Point out every malaria parasite.
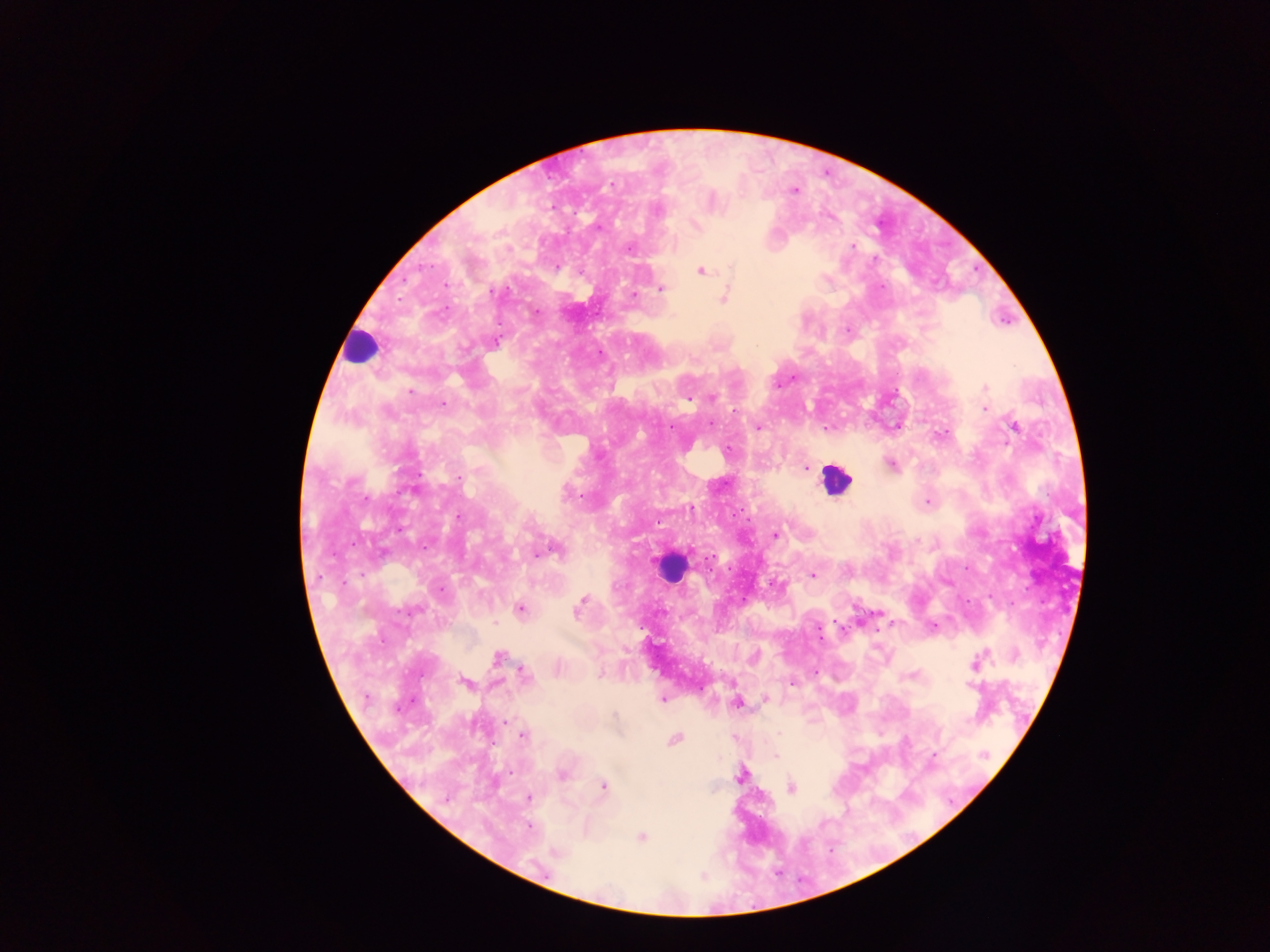
Approximate centers as {x, y} in pixels.
Malaria parasites: {795, 191}, {658, 211}, {695, 225}, {853, 246}, {628, 248}, {557, 267}, {700, 271}, {661, 289}, {633, 295}, {724, 298}, {537, 311}, {846, 330}, {496, 342}, {985, 388}, {410, 390}, {713, 398}, {687, 399}, {443, 404}, {985, 408}, {1014, 426}, {758, 428}, {728, 450}, {891, 464}, {805, 467}, {459, 478}, {413, 489}, {566, 494}, {927, 502}, {459, 517}, {776, 534}, {556, 551}, {537, 555}, {712, 558}, {812, 574}, {441, 589}, {583, 599}, {520, 609}, {412, 610}, {577, 612}, {933, 627}, {497, 658}, {974, 663}, {524, 672}, {815, 672}, {601, 673}, {465, 682}, {792, 683}, {971, 684}, {663, 699}, {765, 699}, {737, 703}, {615, 715}, {506, 722}, {779, 733}, {522, 736}, {674, 739}, {934, 754}, {775, 755}, {985, 755}, {561, 774}, {739, 776}, {604, 785}, {791, 788}, {528, 798}, {530, 827}, {641, 837}, {557, 852}.

Leukocyte locations: {360, 346}, {835, 480}, {669, 567}. Image is 1270×952 pixels. Thick blood film. Mobile-phone photograph taken through the microscope. One field of view. Collected in Ghana.